Name the parasite shown.
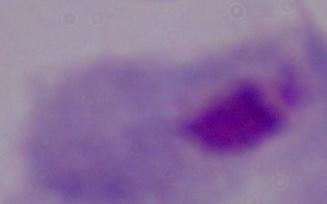
A trichomonad.

Summary:
  - Modality: photomicrograph
  - Magnification: 1000x